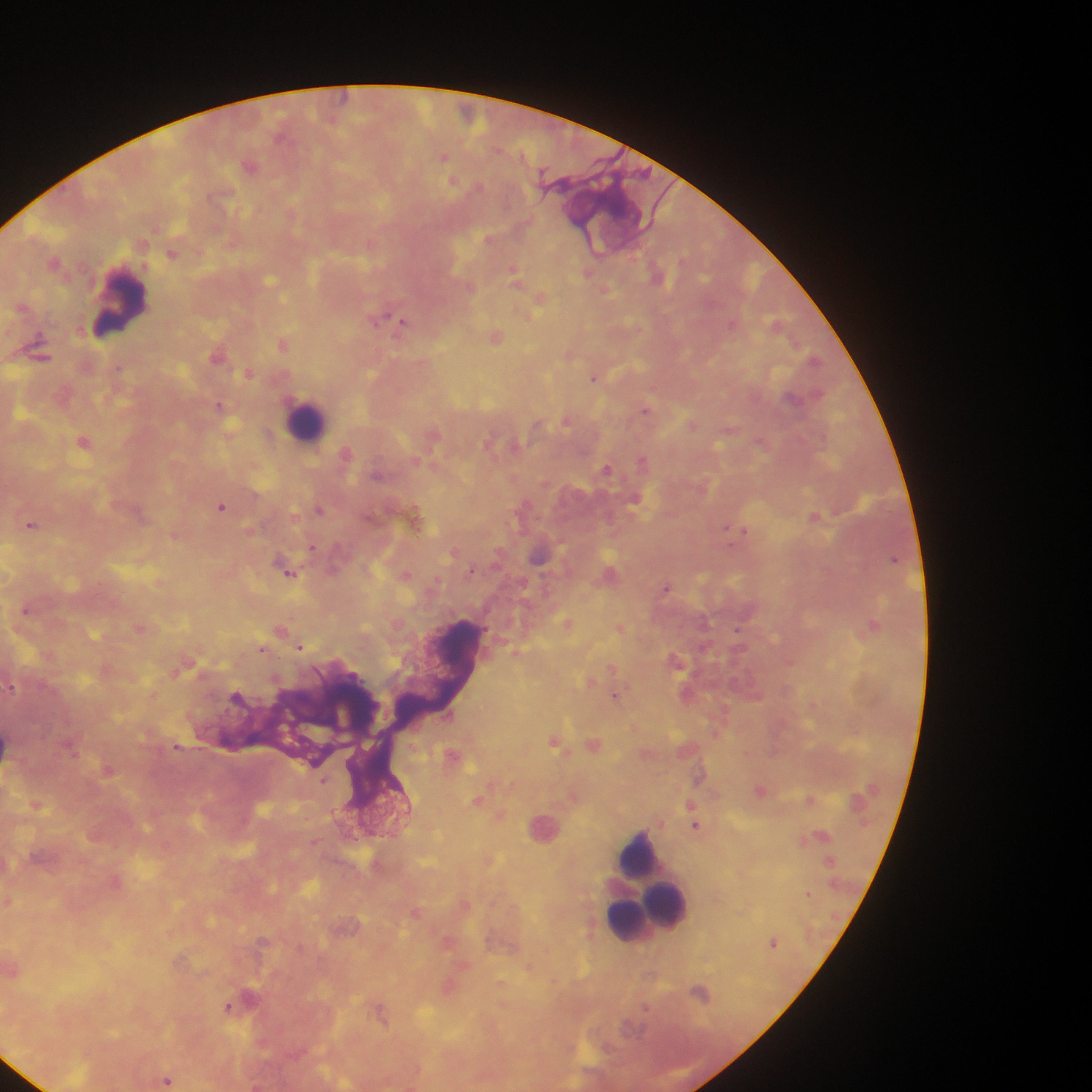
leukocyte locations = approximate centers as {x, y} in pixels: {117, 304}, {307, 425}, {640, 852}, {653, 913}
field of view = single
preparation = thick blood film
Plasmodium parasite locations = approximate centers as {x, y} in pixels: {346, 97}, {444, 157}, {172, 253}, {513, 270}, {589, 272}, {540, 298}, {380, 321}, {402, 322}, {731, 325}, {497, 338}, {282, 344}, {594, 377}, {647, 410}, {566, 422}, {760, 439}, {642, 460}, {606, 468}, {222, 507}, {815, 516}, {33, 524}, {726, 527}, {743, 529}, {731, 546}, {666, 587}, {738, 631}, {301, 648}, {263, 649}, {612, 666}, {12, 686}, {613, 693}, {176, 745}, {810, 799}, {690, 805}, {695, 825}, {808, 894}, {417, 910}, {773, 942}, {700, 992}, {646, 1006}, {228, 1007}, {379, 1009}, {167, 1081}
capture = mobile-phone photograph through a microscope
image size = 1092×1092 pixels
country = Ghana